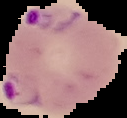
{
  "preparation": "thin blood smear",
  "image_type": "segmented cell region on a black background",
  "malaria_status": "parasitized",
  "image_size": "127×118 pixels"
}